Assess the morphology of the red blood cells.
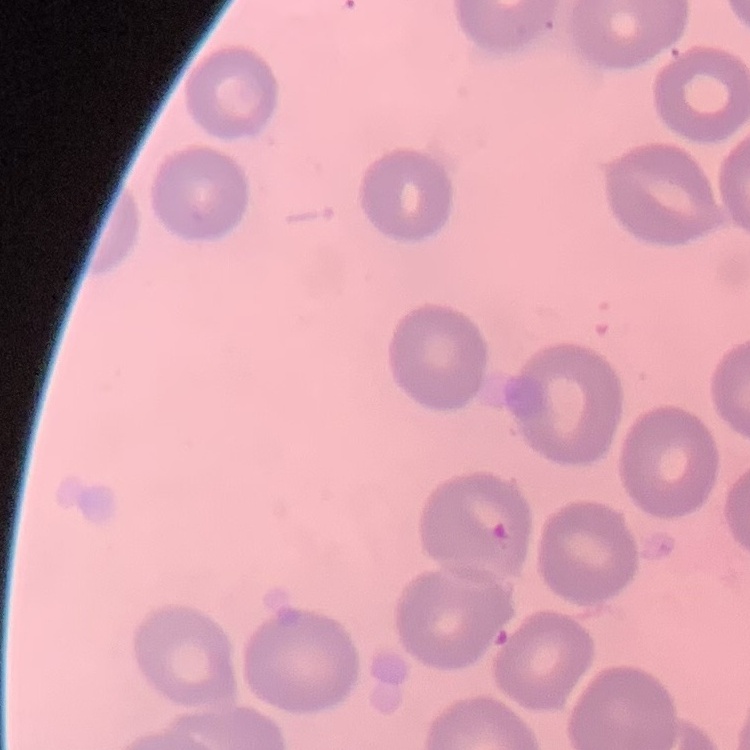
They show no rouleaux formation.

Summary:
  - Preparation: thin blood film
  - Stain: Field's or Giemsa
  - Image type: square crop of a larger photomicrograph